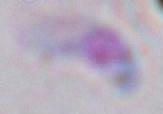

modality = micrograph
magnification = 1000x
identification = Toxoplasma gondii